Outline each blood parasite and name the species.
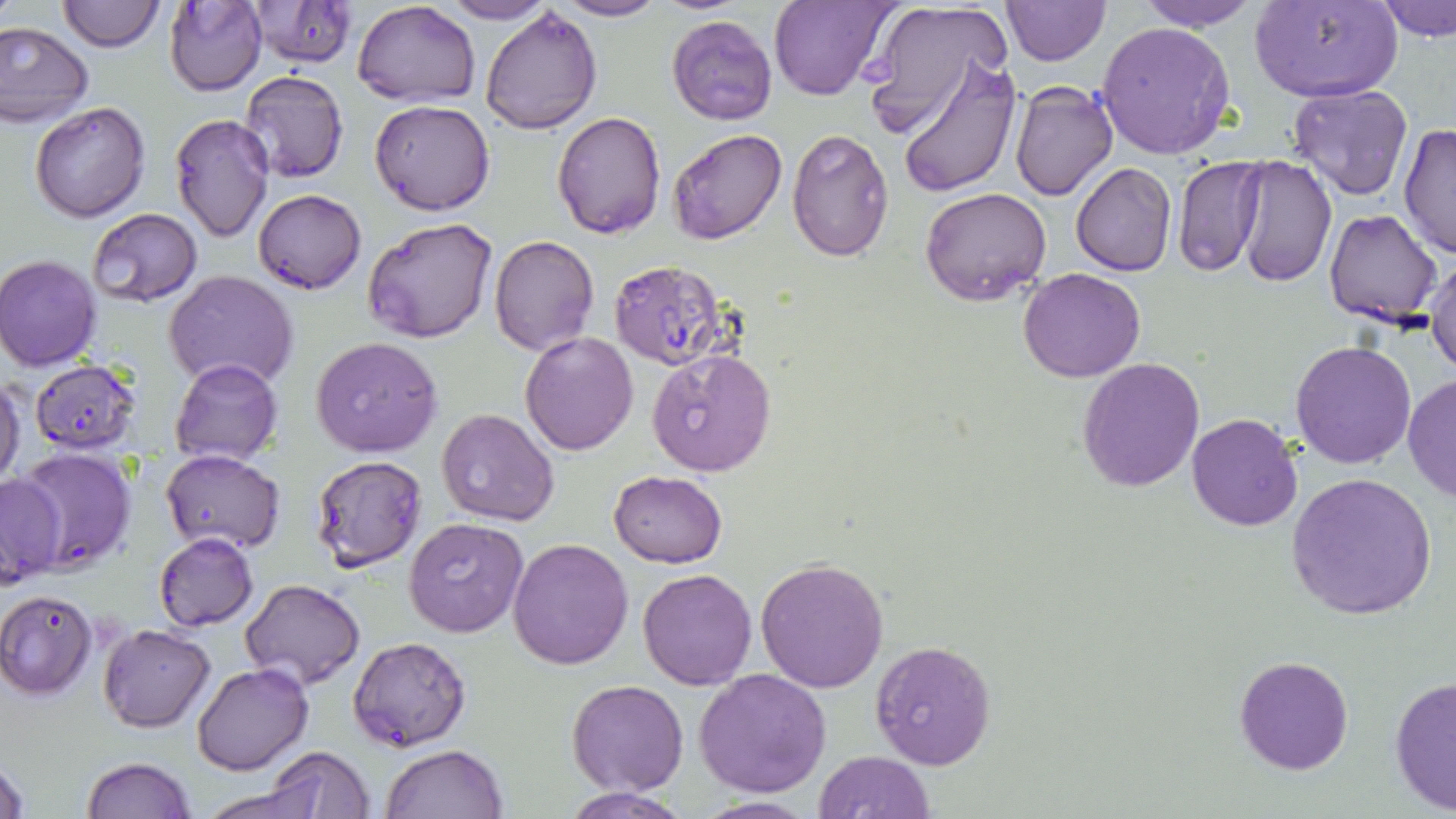
Approximate bounding boxes as [x1, y1, x2, y2] in pixels.
Plasmodium falciparum-infected red blood cells: [608, 257, 730, 370].
No Plasmodium ovale, Plasmodium malariae, Plasmodium vivax, Babesia divergens, or Trypanosoma brucei observed.

Summary:
  - Uninfected red blood cell locations: [56, 0, 163, 51], [163, 0, 267, 96], [549, 0, 666, 22], [770, 0, 895, 102], [859, 0, 1012, 139], [1001, 0, 1109, 65], [1133, 0, 1263, 31], [1254, 0, 1402, 102], [1377, 0, 1456, 42], [248, 1, 358, 70], [354, 1, 480, 106], [438, 1, 558, 24], [479, 7, 602, 134], [667, 15, 777, 126], [0, 21, 95, 127], [1096, 21, 1236, 160], [895, 55, 1020, 198], [239, 69, 350, 184], [1008, 80, 1118, 203], [1288, 82, 1413, 199], [370, 100, 495, 216], [30, 101, 152, 223], [553, 111, 667, 239], [170, 114, 275, 242], [1398, 119, 1456, 260], [666, 128, 786, 246], [787, 128, 895, 263], [1235, 155, 1335, 288], [1173, 156, 1267, 278], [1071, 163, 1176, 276], [919, 186, 1052, 306], [253, 189, 367, 293], [1324, 208, 1444, 329], [84, 209, 203, 309], [362, 215, 497, 342], [490, 235, 599, 357], [1427, 248, 1456, 378], [1, 255, 102, 370], [1019, 267, 1146, 382], [164, 271, 299, 391], [518, 332, 638, 456], [311, 336, 443, 457], [1291, 339, 1416, 468], [647, 348, 778, 476], [1076, 356, 1204, 491], [170, 358, 284, 466], [28, 360, 143, 453], [1403, 373, 1456, 504], [0, 375, 26, 488], [436, 409, 561, 528], [1186, 413, 1303, 531], [14, 447, 138, 573], [161, 449, 285, 553], [310, 455, 429, 571], [608, 471, 728, 567], [0, 472, 66, 587], [1288, 473, 1437, 620], [404, 518, 530, 637], [153, 532, 259, 631], [507, 537, 634, 670], [754, 556, 889, 691], [638, 569, 757, 690], [239, 578, 365, 688], [0, 588, 98, 699], [98, 623, 215, 732], [349, 636, 470, 750], [870, 640, 997, 770], [1234, 654, 1354, 775], [190, 663, 313, 775], [693, 668, 834, 797], [1389, 672, 1455, 817], [567, 679, 689, 795], [380, 743, 508, 819], [265, 746, 376, 818], [813, 751, 935, 819], [1, 753, 29, 819], [82, 757, 197, 818], [196, 784, 330, 819], [564, 786, 689, 818], [690, 795, 821, 817]
  - Slide-level diagnosis: Plasmodium falciparum
  - Modality: light microscopy
  - Image size: 1456×819 pixels
  - Stain: May-Grünwald-Giemsa
  - Preparation: thin blood smear
  - Magnification: 1000x
  - Field of view: single